Assess this cell for malaria.
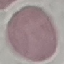
It is uninfected.

Cell patch, automatically extracted from a larger field of view and resized to 64 × 64 pixels. Giemsa-stained preparation. Thin blood smear. Acquired by smartphone through the microscope eyepiece.